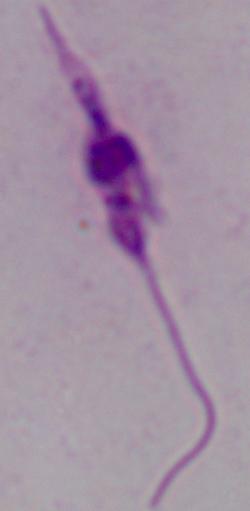

identification = Leishmania
magnification = 1000x
modality = photomicrograph